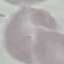
result = negative for malaria parasites
preparation = thin blood smear
image type = automatically extracted cell patch, resized to 64 × 64 pixels
capture = smartphone camera at the microscope eyepiece
stain = Giemsa